Identify the cell.
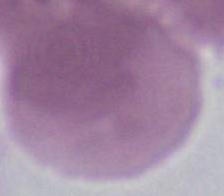
This is an erythrocyte.

{
  "magnification": "1000x",
  "modality": "photomicrograph"
}